Classify this cell by malaria status.
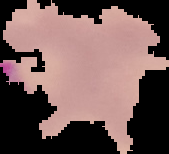

Parasitized.

Image is 169×154 pixels. The area outside the segmented cell region is set to black. From a thin blood film.